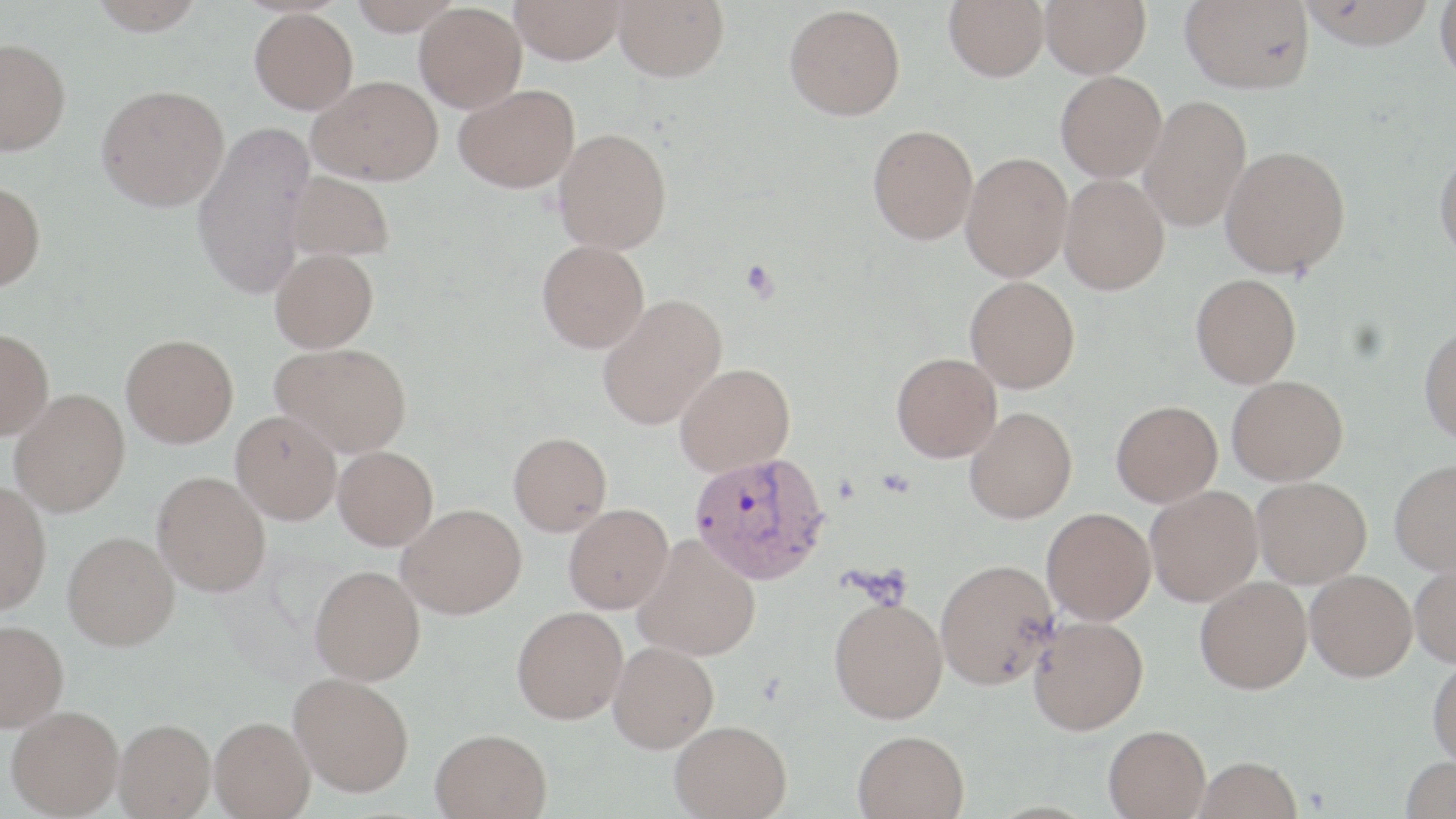
slide_level_diagnosis: Plasmodium vivax
image_size: 1456×819 pixels
platelet_locations: 'approximate bounding boxes as named x1/y1/x2/y2 corners in pixels: (x1=740, y1=259, x2=779, y2=302)'
magnification: 1000x
modality: optical microscopy
field_of_view: one of a larger specimen
uninfected_red_blood_cell_locations: 'approximate bounding boxes as named x1/y1/x2/y2 corners in pixels: (x1=87, y1=0, x2=206, y2=35), (x1=348, y1=0, x2=462, y2=35), (x1=510, y1=0, x2=625, y2=64), (x1=614, y1=0, x2=729, y2=82), (x1=944, y1=0, x2=1049, y2=81), (x1=1040, y1=0, x2=1151, y2=77), (x1=1180, y1=0, x2=1315, y2=93), (x1=1300, y1=0, x2=1436, y2=50), (x1=1434, y1=0, x2=1456, y2=83), (x1=414, y1=3, x2=527, y2=112), (x1=784, y1=4, x2=905, y2=120), (x1=249, y1=8, x2=358, y2=113), (x1=0, y1=37, x2=71, y2=155), (x1=1055, y1=71, x2=1167, y2=182), (x1=309, y1=75, x2=442, y2=185), (x1=96, y1=84, x2=229, y2=211), (x1=454, y1=84, x2=580, y2=192), (x1=1139, y1=94, x2=1251, y2=231), (x1=191, y1=120, x2=315, y2=300), (x1=867, y1=125, x2=978, y2=245), (x1=554, y1=127, x2=672, y2=253), (x1=1221, y1=145, x2=1350, y2=277), (x1=1433, y1=147, x2=1456, y2=264), (x1=961, y1=151, x2=1073, y2=281), (x1=287, y1=171, x2=394, y2=262), (x1=1059, y1=173, x2=1170, y2=294), (x1=0, y1=180, x2=46, y2=291), (x1=536, y1=240, x2=649, y2=353), (x1=270, y1=248, x2=378, y2=352), (x1=1191, y1=274, x2=1301, y2=388), (x1=965, y1=276, x2=1080, y2=393), (x1=596, y1=293, x2=727, y2=430), (x1=1419, y1=324, x2=1456, y2=446), (x1=0, y1=328, x2=54, y2=439), (x1=121, y1=334, x2=239, y2=447), (x1=271, y1=342, x2=412, y2=456), (x1=892, y1=352, x2=1001, y2=462), (x1=674, y1=363, x2=795, y2=477), (x1=1227, y1=375, x2=1348, y2=485), (x1=9, y1=389, x2=130, y2=516), (x1=1111, y1=400, x2=1222, y2=507), (x1=965, y1=406, x2=1077, y2=523), (x1=231, y1=410, x2=342, y2=524), (x1=509, y1=432, x2=612, y2=535), (x1=333, y1=446, x2=438, y2=550), (x1=1390, y1=458, x2=1456, y2=574), (x1=153, y1=471, x2=271, y2=596), (x1=1252, y1=477, x2=1372, y2=588), (x1=0, y1=481, x2=51, y2=615), (x1=1145, y1=485, x2=1263, y2=606), (x1=398, y1=503, x2=527, y2=619), (x1=563, y1=504, x2=673, y2=614), (x1=1042, y1=507, x2=1156, y2=625), (x1=63, y1=530, x2=179, y2=650), (x1=633, y1=535, x2=761, y2=661), (x1=935, y1=558, x2=1058, y2=690), (x1=1409, y1=559, x2=1456, y2=667), (x1=310, y1=565, x2=426, y2=685), (x1=1306, y1=569, x2=1417, y2=681), (x1=1195, y1=576, x2=1312, y2=694), (x1=829, y1=596, x2=948, y2=723), (x1=512, y1=606, x2=628, y2=723), (x1=1028, y1=615, x2=1148, y2=735), (x1=0, y1=620, x2=69, y2=730), (x1=609, y1=642, x2=719, y2=753), (x1=1427, y1=656, x2=1456, y2=767), (x1=289, y1=672, x2=414, y2=796), (x1=6, y1=705, x2=124, y2=817), (x1=210, y1=716, x2=314, y2=818), (x1=114, y1=718, x2=216, y2=818), (x1=669, y1=719, x2=791, y2=818), (x1=1103, y1=724, x2=1211, y2=818), (x1=431, y1=728, x2=551, y2=818), (x1=853, y1=729, x2=969, y2=819), (x1=1400, y1=755, x2=1456, y2=818), (x1=1194, y1=756, x2=1303, y2=819)'
plasmodium_vivax_infected_red_blood_cell_locations: 'approximate bounding boxes as named x1/y1/x2/y2 corners in pixels: (x1=689, y1=452, x2=830, y2=584)'
stain: May-Grünwald-Giemsa
preparation: thin blood film